Name the parasite shown.
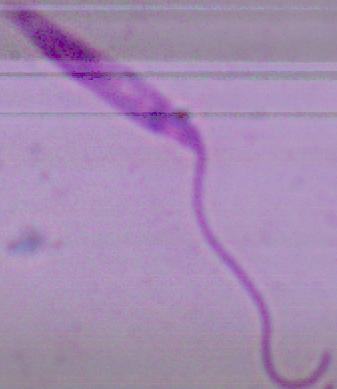

This is Leishmania.

Photomicrograph. Captured at 1000x magnification.